Report the malaria status of this cell.
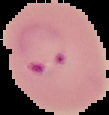
Parasitized.

Image is 109×115 pixels. From a thin blood smear. The area outside the segmented cell region is set to black.